Name the blood parasite species.
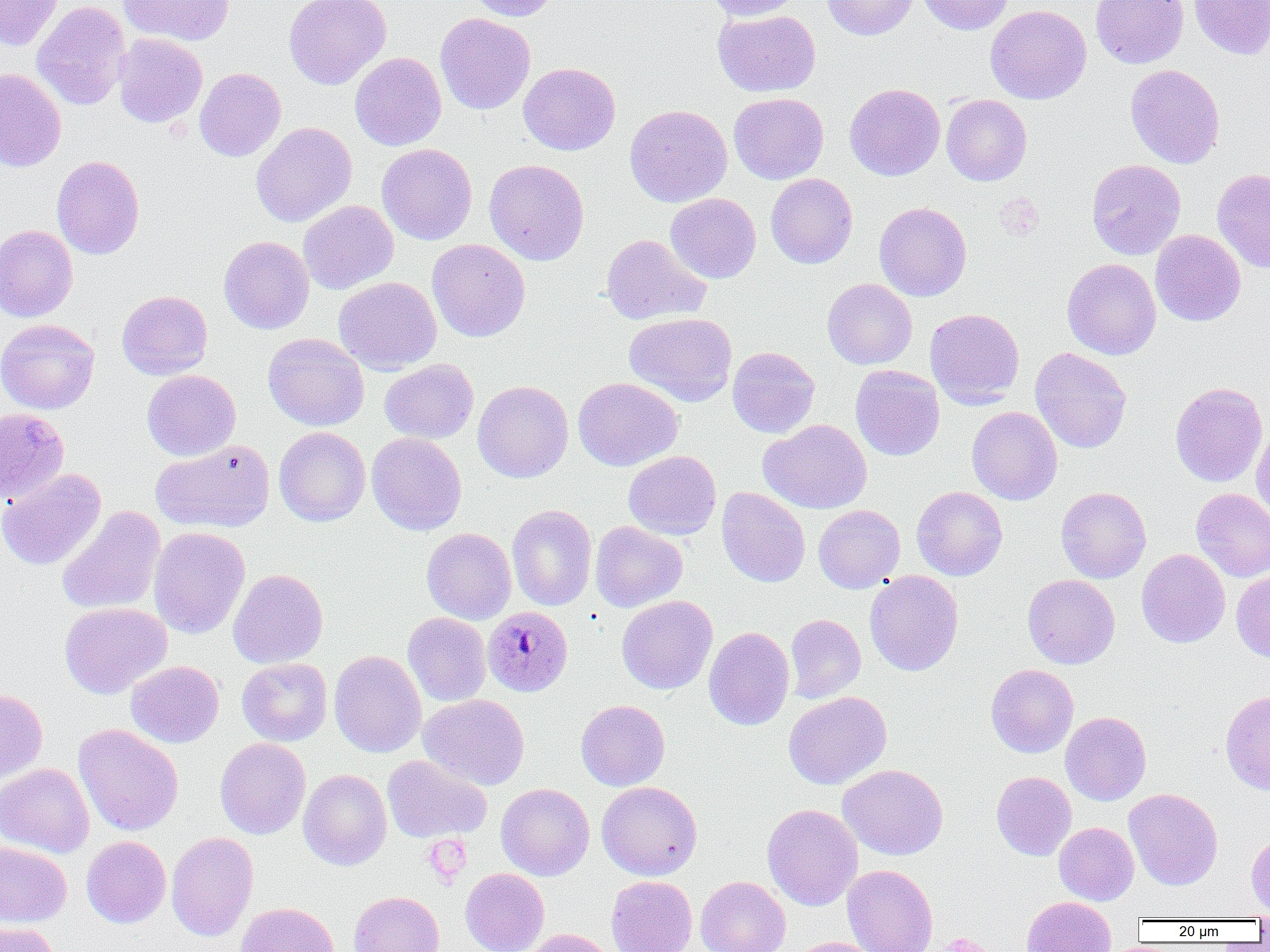
Plasmodium malariae.

platelet locations = approximate bounding boxes as (x1,y1)-(x2,y2) corner pairs in pixels: (996,193)-(1045,241), (423,834)-(472,887), (932,933)-(995,952)
modality = light microscopy
Plasmodium malariae-infected red blood cell locations = approximate bounding boxes as (x1,y1)-(x2,y2) corner pairs in pixels: (483,606)-(573,697)
image size = 1270×952 pixels
magnification = 1000x
field of view = one of a larger specimen
uninfected red blood cell locations = approximate bounding boxes as (x1,y1)-(x2,y2) corner pairs in pixels: (0,0)-(63,51), (117,0)-(235,46), (283,0)-(391,90), (464,0)-(561,21), (703,0)-(804,21), (822,0)-(918,40), (917,0)-(1014,35), (1090,0)-(1188,68), (1189,0)-(1270,60), (31,1)-(130,111), (985,4)-(1092,104), (712,9)-(821,97), (435,13)-(535,114), (113,33)-(207,128), (350,52)-(446,151), (518,62)-(620,155), (1124,64)-(1225,168), (195,67)-(286,162), (0,68)-(66,171), (844,83)-(945,181), (728,92)-(828,184), (941,95)-(1032,185), (624,104)-(732,207), (251,122)-(357,227), (377,143)-(477,245), (51,155)-(145,260), (484,159)-(589,265), (1086,159)-(1186,259), (1212,168)-(1270,273), (765,174)-(857,268), (665,193)-(761,283), (298,200)-(398,294), (874,202)-(971,301), (0,224)-(78,322), (1150,230)-(1246,326), (600,234)-(711,326), (219,236)-(314,334), (427,239)-(530,342), (1061,258)-(1161,359), (334,276)-(442,375), (822,278)-(917,369), (117,290)-(213,380), (925,308)-(1025,408), (624,312)-(737,406), (0,319)-(100,414), (263,333)-(369,431), (727,346)-(819,438), (1030,347)-(1132,453), (380,359)-(479,443), (851,365)-(944,461), (142,369)-(241,461), (573,377)-(683,471), (472,380)-(573,483), (1170,382)-(1267,487), (967,406)-(1062,505), (0,407)-(69,505), (759,419)-(871,514), (1252,422)-(1270,526), (274,427)-(370,526), (366,432)-(467,535), (151,439)-(275,532), (623,451)-(721,540), (0,469)-(106,570), (912,486)-(1008,581), (716,487)-(810,587), (1056,487)-(1151,583), (1191,488)-(1270,582), (506,504)-(597,611), (813,505)-(905,593), (57,506)-(166,615), (590,520)-(688,612), (148,526)-(250,638), (421,527)-(517,624), (1136,549)-(1230,648), (228,568)-(328,668), (1231,569)-(1270,662), (864,570)-(963,676), (1023,574)-(1120,669), (616,595)-(717,694), (59,602)-(171,698), (402,612)-(491,706), (785,613)-(866,703), (704,626)-(794,730), (329,650)-(426,758), (236,658)-(332,746), (126,660)-(224,747), (986,664)-(1078,758), (0,689)-(48,781), (783,691)-(892,789), (1220,691)-(1270,795), (418,694)-(530,790), (576,700)-(670,790), (1061,712)-(1151,805), (74,724)-(183,836), (215,738)-(311,839), (382,755)-(492,842), (0,763)-(94,858), (837,764)-(949,860), (298,769)-(392,870), (991,771)-(1076,860), (597,781)-(702,880), (496,783)-(594,881), (1124,788)-(1223,890), (762,804)-(862,910), (1054,822)-(1139,905), (1246,831)-(1270,917), (166,832)-(259,942), (81,836)-(171,928), (0,841)-(72,927), (843,864)-(938,952), (460,868)-(549,952), (606,875)-(697,952), (696,876)-(790,952), (349,891)-(444,952), (1021,896)-(1116,952), (235,902)-(340,952), (0,921)-(60,952), (521,928)-(621,952), (788,937)-(883,952)
preparation = thin blood smear